Outline each blood parasite and name the species.
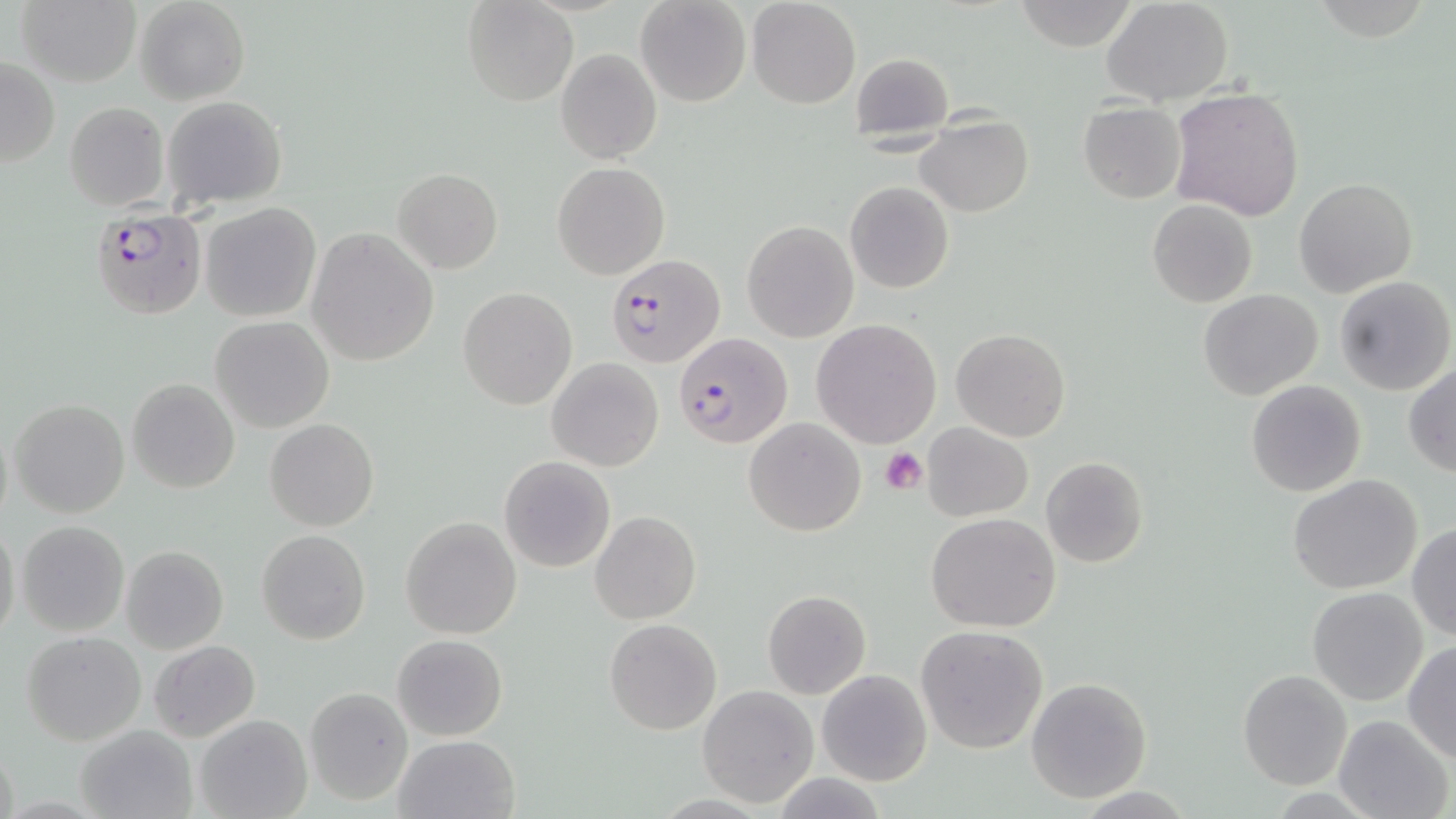
Approximate bounding boxes as (x1, y1, x2, y2) in pixels.
Plasmodium falciparum-infected red blood cells: (91, 209, 207, 319), (606, 255, 725, 367), (673, 332, 793, 449).
No Plasmodium ovale, Plasmodium malariae, Plasmodium vivax, Babesia divergens, or Trypanosoma brucei observed.

slide-level diagnosis = Plasmodium falciparum
stain = May-Grünwald-Giemsa
magnification = 1000x
uninfected red blood cell locations = approximate bounding boxes as (x1, y1, x2, y2) in pixels: (16, 0, 141, 87), (134, 0, 249, 106), (462, 0, 576, 108), (636, 0, 751, 107), (747, 0, 860, 109), (1102, 0, 1235, 106), (1007, 1, 1141, 47), (555, 48, 661, 164), (849, 53, 952, 138), (0, 57, 60, 168), (1171, 87, 1306, 221), (162, 97, 289, 207), (63, 103, 169, 212), (1078, 103, 1185, 202), (917, 116, 1033, 218), (552, 161, 670, 280), (394, 167, 503, 273), (1292, 177, 1417, 298), (845, 181, 954, 293), (1148, 199, 1257, 308), (199, 202, 322, 323), (742, 220, 859, 342), (307, 227, 439, 367), (1333, 274, 1455, 395), (458, 287, 576, 408), (1199, 288, 1324, 401), (211, 316, 334, 432), (812, 319, 942, 448), (951, 327, 1070, 441), (546, 357, 664, 471), (1404, 363, 1456, 476), (126, 378, 240, 494), (1245, 379, 1366, 497), (9, 398, 129, 519), (0, 417, 13, 534), (743, 417, 867, 537), (265, 418, 378, 531), (923, 423, 1033, 520), (498, 456, 616, 572), (1041, 457, 1150, 569), (1287, 474, 1424, 593), (591, 510, 700, 624), (925, 513, 1061, 631), (401, 517, 522, 639), (0, 520, 21, 644), (15, 520, 130, 637), (1408, 522, 1456, 640), (256, 530, 371, 646), (121, 545, 229, 654), (1307, 586, 1430, 706), (763, 590, 871, 699), (604, 619, 722, 735), (915, 624, 1051, 755), (21, 630, 146, 745), (391, 634, 508, 740), (148, 639, 261, 744), (1403, 640, 1456, 764), (816, 669, 932, 786), (1238, 669, 1353, 789), (1025, 676, 1152, 804), (697, 686, 817, 806), (303, 687, 412, 805), (195, 714, 312, 819), (1333, 714, 1451, 819), (74, 723, 197, 819), (394, 734, 518, 819), (771, 774, 888, 818)
platelet locations = approximate bounding boxes as (x1, y1, x2, y2) in pixels: (881, 447, 929, 496)
preparation = thin blood smear
field of view = one of a larger specimen
image size = 1456×819 pixels
modality = optical microscopy